Identify the parasite.
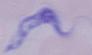
This is a trypanosome.

magnification = 1000x
modality = photomicrograph